Locate every blood parasite and identify its species.
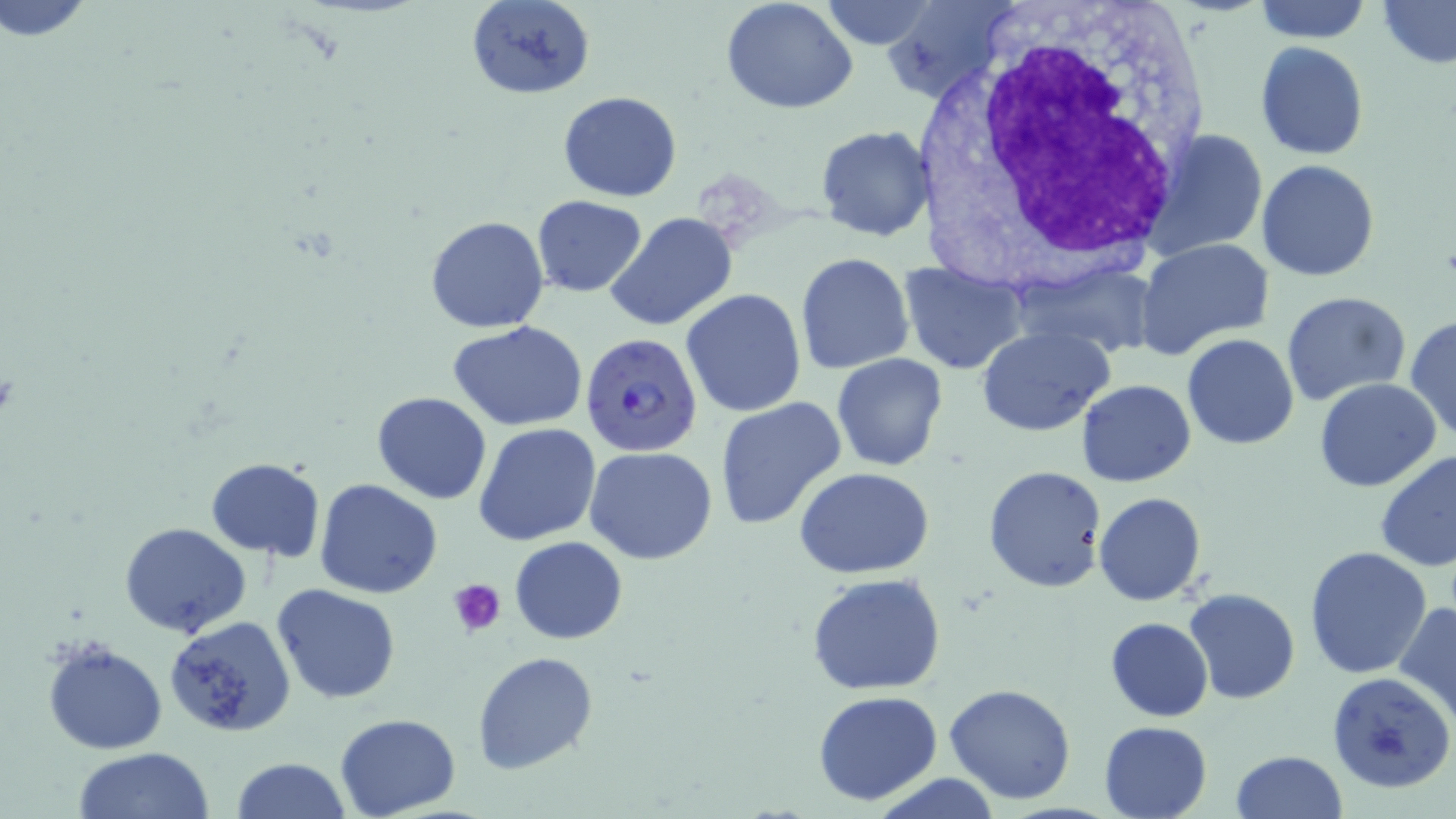

Approximate bounding boxes as (x1,y1)-(x2,y2) corner pairs in pixels.
Plasmodium falciparum-infected red blood cells: (581,332)-(703,456).
No Plasmodium ovale, Plasmodium malariae, Plasmodium vivax, Babesia divergens, or Trypanosoma brucei observed.

slide-level diagnosis = Plasmodium falciparum
stain = May-Grünwald-Giemsa
uninfected red blood cell locations = approximate bounding boxes as (x1,y1)-(x2,y2) corner pairs in pixels: (1,0)-(94,42), (465,0)-(596,101), (720,0)-(858,114), (818,0)-(941,51), (883,0)-(1017,102), (1254,0)-(1372,43), (1376,0)-(1456,68), (1254,41)-(1369,160), (557,92)-(682,202), (815,125)-(933,242), (1144,129)-(1266,258), (1256,159)-(1380,281), (532,196)-(648,296), (603,211)-(738,332), (425,214)-(548,332), (1136,238)-(1275,359), (794,253)-(914,376), (900,259)-(1025,374), (680,289)-(806,417), (1281,291)-(1411,408), (1407,316)-(1456,443), (448,321)-(591,432), (976,326)-(1112,435), (1181,333)-(1299,450), (831,352)-(949,471), (1314,378)-(1442,492), (1077,380)-(1196,486), (372,392)-(492,505), (714,397)-(847,529), (474,423)-(602,547), (585,447)-(718,565), (1375,449)-(1456,572), (206,458)-(326,560), (983,465)-(1107,592), (793,467)-(936,579), (315,478)-(444,599), (1092,492)-(1206,606), (121,522)-(252,639), (509,537)-(627,644), (1304,547)-(1432,680), (805,571)-(949,696), (273,584)-(401,702), (1183,588)-(1299,705), (1397,600)-(1456,722), (164,615)-(297,737), (1105,617)-(1214,721), (40,636)-(169,755), (472,651)-(596,774), (1327,671)-(1456,794), (944,682)-(1076,804), (813,691)-(943,806), (333,713)-(461,819), (1097,720)-(1213,819), (72,748)-(214,819), (1229,749)-(1347,819), (230,757)-(352,819), (872,774)-(1002,818)
white blood cell locations = approximate bounding boxes as (x1,y1)-(x2,y2) corner pairs in pixels: (916,3)-(1213,299)
preparation = thin blood film
image size = 1456×819 pixels
magnification = 1000x
modality = optical microscopy
platelet locations = approximate bounding boxes as (x1,y1)-(x2,y2) corner pairs in pixels: (448,578)-(507,634)
field of view = one of a larger specimen